Assess this cell for malaria.
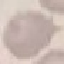

It is uninfected.

{
  "image_type": "automatically extracted cell patch, resized to 64 × 64 pixels",
  "capture": "smartphone camera at the microscope eyepiece",
  "stain": "Giemsa",
  "preparation": "thin blood film"
}